Assess this cell for malaria.
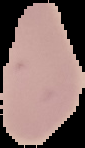

It is uninfected.

Segmented cell region on a black background. From a thin blood film. Image is 85×148 pixels.